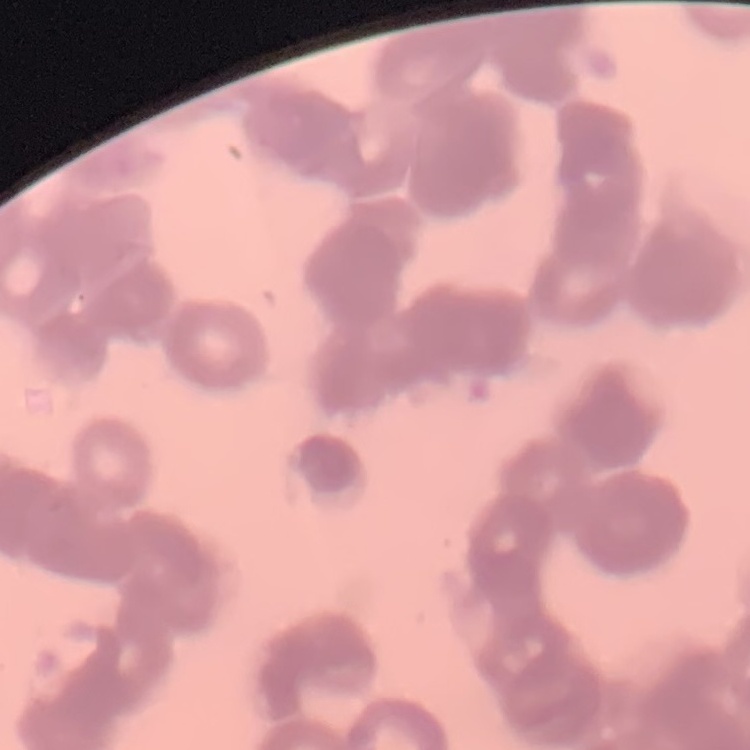

erythrocyte morphology = rouleaux formation
stain = Field's or Giemsa
image type = square crop of a larger photomicrograph
preparation = thin blood smear